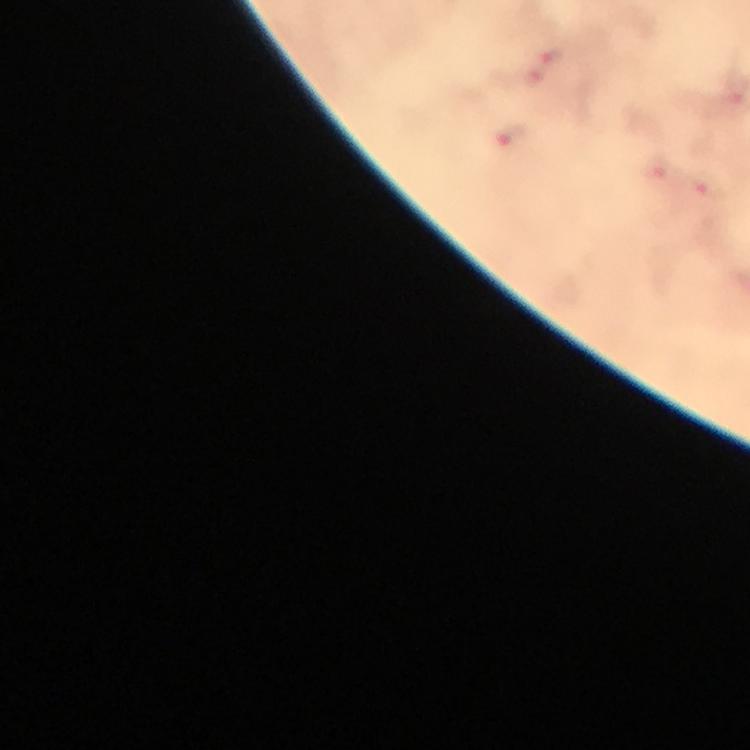
Approximate centers as [x, y] in pixels.
Summary:
  - Plasmodium parasite locations: [552, 54], [511, 133], [658, 167], [709, 185]
  - Cropped from: one field of view
  - Magnification: 100x
  - Capture: smartphone camera through the microscope
  - Immersion oil: used
  - Context: from a malaria diagnostic workup
  - Preparation: thick blood smear
  - Stain: Giemsa
  - Image size: 750×750 pixels